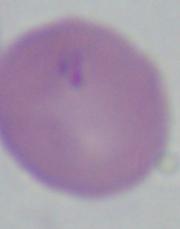

modality: micrograph
magnification: 1000x
identification: Babesia